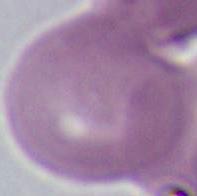

Micrograph. A red blood cell is seen. Captured at 1000x magnification.